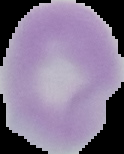

Image is 124×154 pixels. The area outside the segmented cell region is set to black. Malaria status: uninfected. From a thin blood smear.